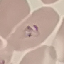
Result: malaria parasites identified. Thin blood film. Automatically extracted cell patch, resized to 64 × 64 pixels. Photographed with a smartphone camera at the microscope eyepiece. Giemsa stain.